Name the blood parasite species.
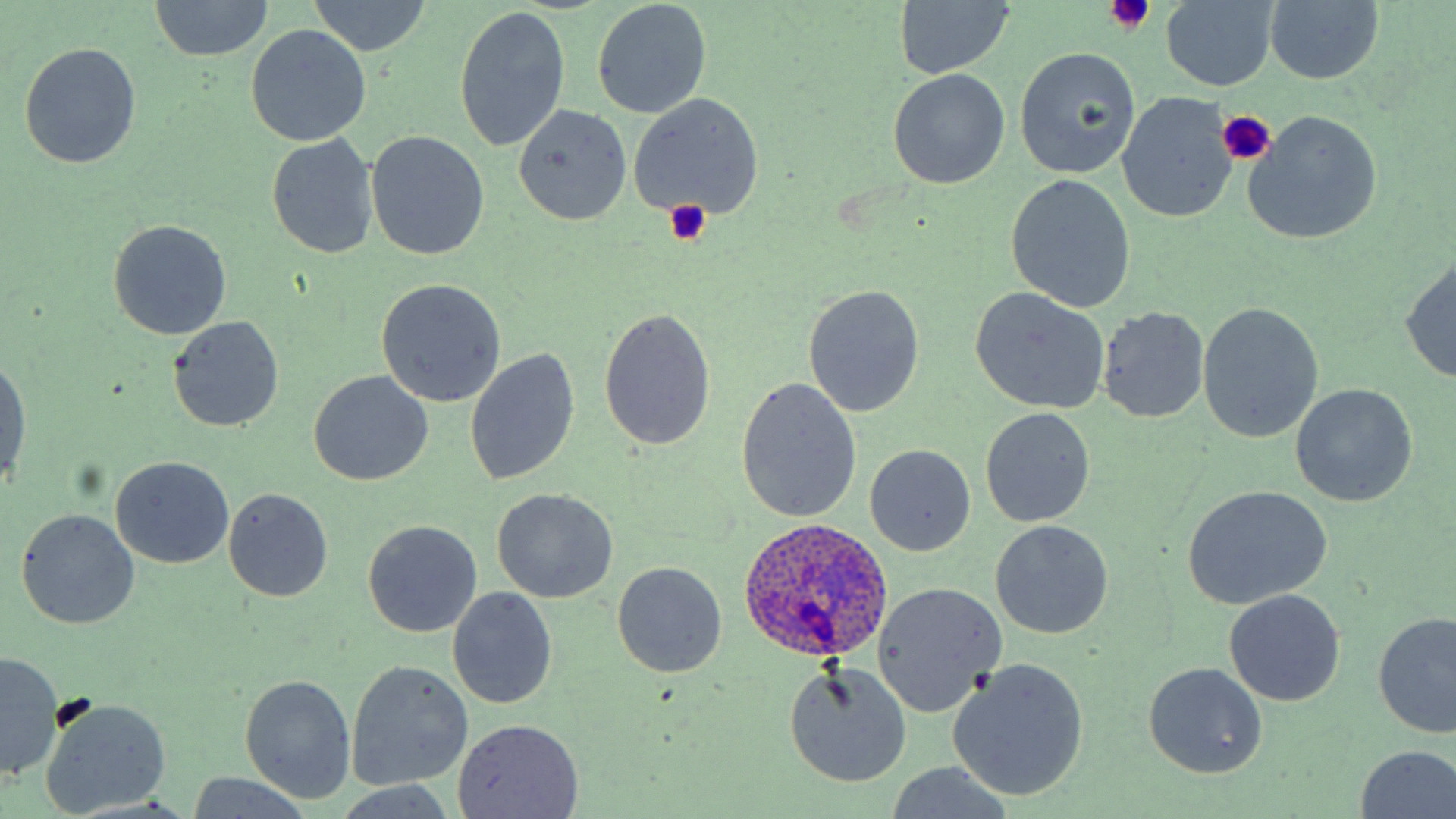
Plasmodium ovale.

Approximate bounding boxes as named x1/y1/x2/y2 corners in pixels. Uninfected red blood cell locations: (x1=149, y1=0, x2=276, y2=62), (x1=892, y1=0, x2=1013, y2=81), (x1=304, y1=1, x2=433, y2=56), (x1=592, y1=1, x2=711, y2=119), (x1=1262, y1=1, x2=1382, y2=86), (x1=1161, y1=2, x2=1279, y2=90), (x1=454, y1=8, x2=570, y2=150), (x1=246, y1=24, x2=372, y2=146), (x1=19, y1=43, x2=141, y2=168), (x1=1014, y1=48, x2=1141, y2=179), (x1=889, y1=69, x2=1009, y2=188), (x1=627, y1=93, x2=764, y2=220), (x1=1118, y1=94, x2=1236, y2=223), (x1=513, y1=104, x2=631, y2=225), (x1=1245, y1=111, x2=1381, y2=244), (x1=365, y1=130, x2=489, y2=259), (x1=267, y1=134, x2=379, y2=257), (x1=1005, y1=175, x2=1136, y2=313), (x1=108, y1=219, x2=232, y2=339), (x1=1399, y1=256, x2=1456, y2=384), (x1=376, y1=280, x2=507, y2=408), (x1=802, y1=285, x2=925, y2=417), (x1=970, y1=288, x2=1108, y2=414), (x1=1198, y1=302, x2=1324, y2=443), (x1=1097, y1=306, x2=1210, y2=423), (x1=598, y1=307, x2=716, y2=453), (x1=168, y1=317, x2=284, y2=434), (x1=464, y1=348, x2=581, y2=486), (x1=1, y1=357, x2=30, y2=488), (x1=308, y1=370, x2=432, y2=487), (x1=736, y1=376, x2=862, y2=524), (x1=1288, y1=383, x2=1419, y2=509), (x1=980, y1=407, x2=1095, y2=528), (x1=865, y1=444, x2=977, y2=556), (x1=110, y1=456, x2=234, y2=568), (x1=1181, y1=486, x2=1332, y2=609), (x1=223, y1=488, x2=333, y2=602), (x1=491, y1=488, x2=618, y2=603), (x1=16, y1=508, x2=140, y2=629), (x1=362, y1=520, x2=481, y2=637), (x1=990, y1=521, x2=1113, y2=640), (x1=611, y1=561, x2=728, y2=678), (x1=872, y1=581, x2=1005, y2=718), (x1=446, y1=587, x2=558, y2=710), (x1=1223, y1=591, x2=1347, y2=706), (x1=1373, y1=612, x2=1456, y2=740), (x1=1, y1=651, x2=64, y2=782), (x1=345, y1=660, x2=474, y2=791), (x1=949, y1=661, x2=1088, y2=801), (x1=1143, y1=661, x2=1267, y2=779), (x1=784, y1=664, x2=912, y2=787), (x1=240, y1=674, x2=356, y2=804), (x1=41, y1=699, x2=173, y2=815), (x1=452, y1=718, x2=585, y2=818), (x1=1353, y1=744, x2=1456, y2=819), (x1=183, y1=773, x2=319, y2=818). Platelet locations: (x1=1103, y1=1, x2=1155, y2=32), (x1=1216, y1=110, x2=1274, y2=165), (x1=661, y1=199, x2=711, y2=247). Plasmodium ovale-infected red blood cell locations: (x1=736, y1=516, x2=896, y2=666). Single field of view. Optical microscopy. May-Grünwald-Giemsa stain. Thin blood smear. Image is 1456×819 pixels. Captured at 1000x magnification.